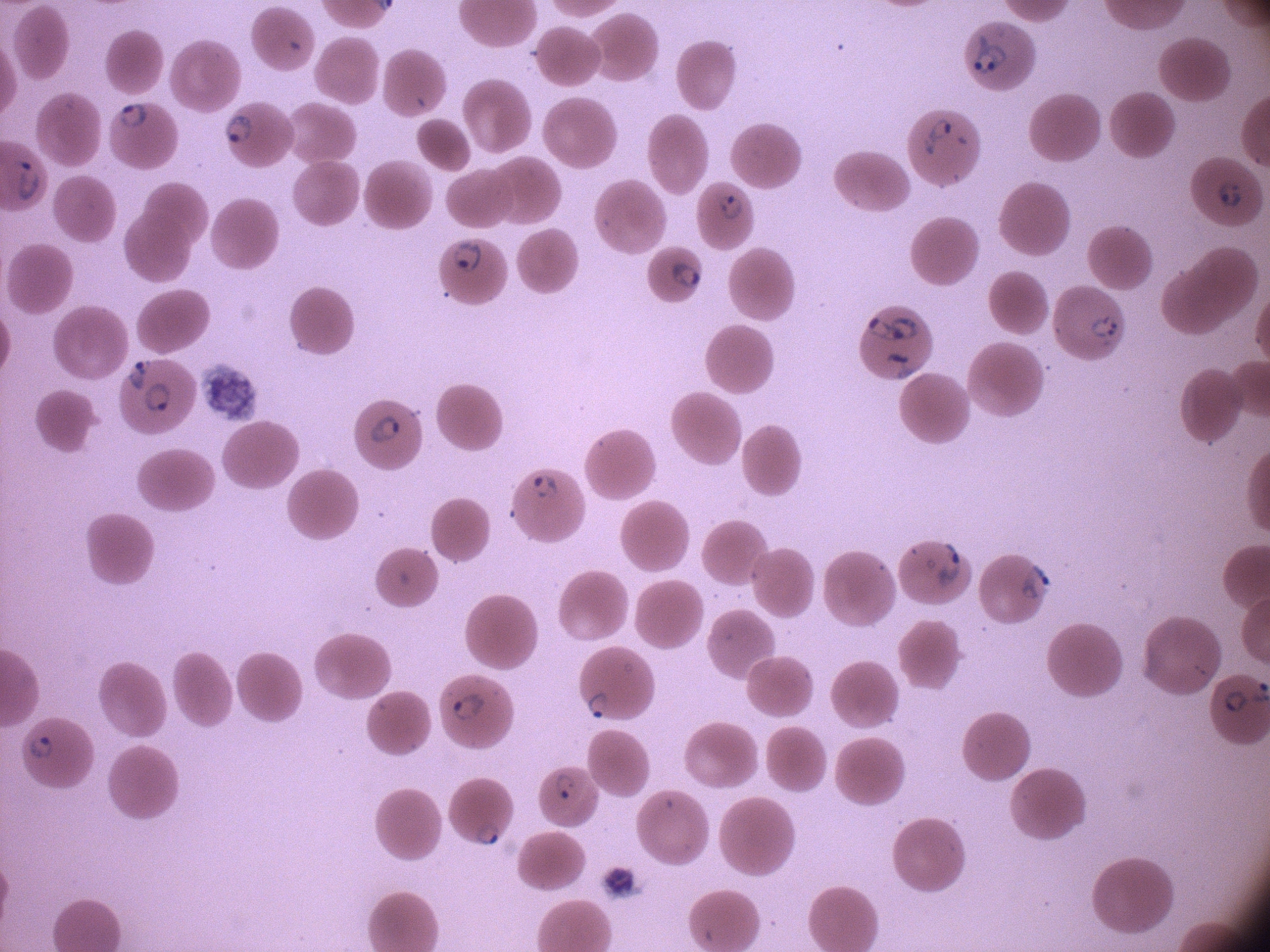

Approximate bounding boxes as named x1/y1/x2/y2 corners in pixels, from the source annotation, which is not necessarily exhaustive. Ring form locations: (x1=966, y1=32, x2=1012, y2=78), (x1=117, y1=100, x2=150, y2=132), (x1=220, y1=111, x2=255, y2=147), (x1=915, y1=115, x2=960, y2=156), (x1=14, y1=156, x2=46, y2=204), (x1=1214, y1=178, x2=1247, y2=213), (x1=709, y1=188, x2=751, y2=225), (x1=447, y1=237, x2=484, y2=277), (x1=663, y1=255, x2=707, y2=300), (x1=894, y1=312, x2=927, y2=344), (x1=1083, y1=312, x2=1123, y2=346), (x1=861, y1=313, x2=898, y2=349), (x1=877, y1=350, x2=925, y2=382), (x1=123, y1=354, x2=155, y2=394), (x1=141, y1=378, x2=172, y2=419), (x1=367, y1=412, x2=402, y2=446), (x1=528, y1=471, x2=561, y2=500), (x1=929, y1=539, x2=966, y2=591), (x1=1019, y1=560, x2=1057, y2=605), (x1=580, y1=689, x2=614, y2=721), (x1=448, y1=691, x2=488, y2=725), (x1=23, y1=732, x2=57, y2=765), (x1=551, y1=768, x2=580, y2=806), (x1=474, y1=820, x2=504, y2=850). One field from this slide. Giemsa-stained preparation. Species: Plasmodium falciparum. Thin blood smear. Leica DM2000 optical microscope with a built-in camera. 100x magnification. Image is 1270×952 pixels.